Give the position of every leukocyte visible.
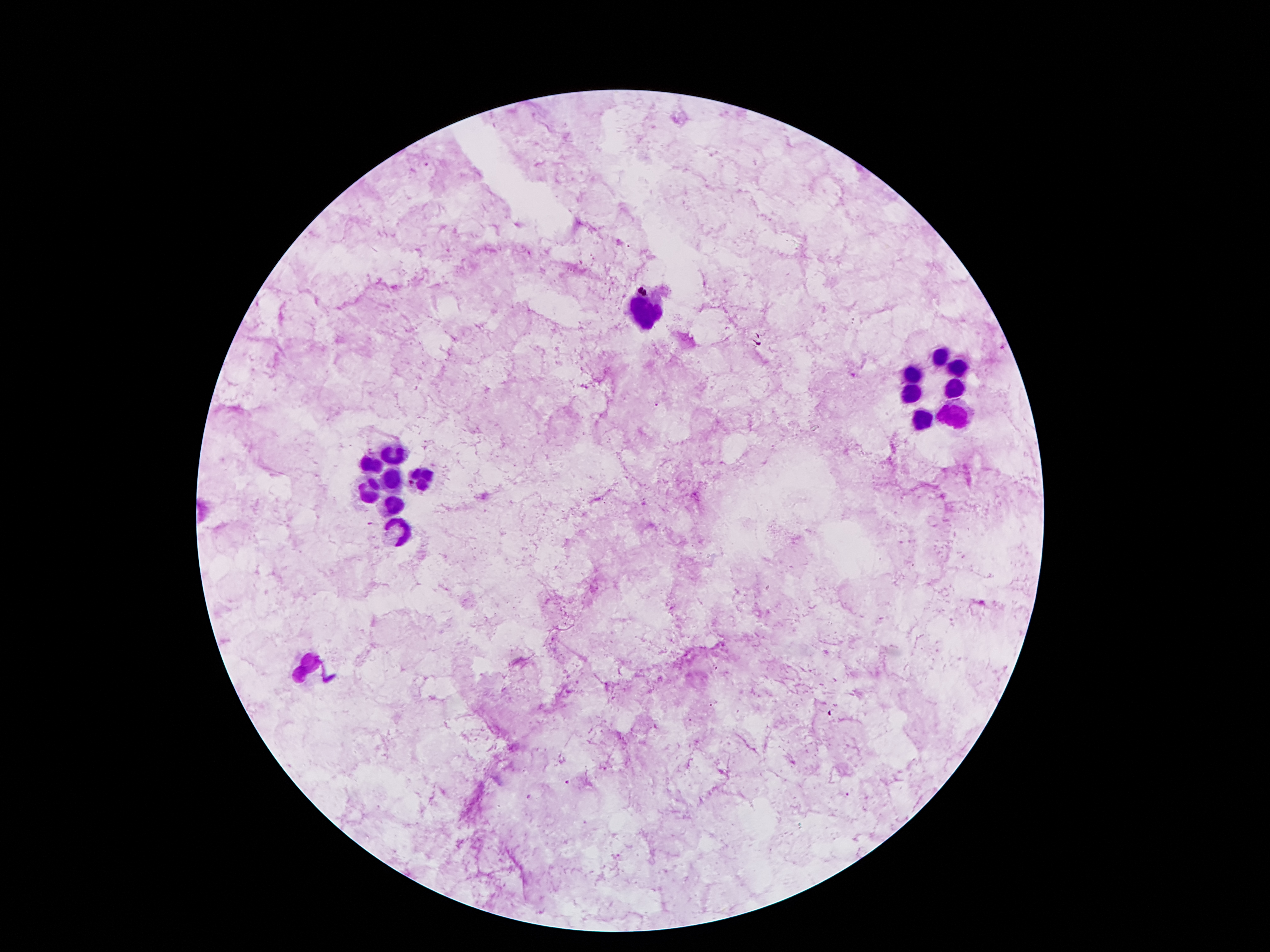

Approximate centers as (x, y) in pixels.
Leukocytes: (646, 312), (940, 356), (954, 370), (912, 373), (910, 391), (956, 391), (956, 410), (923, 417), (394, 457), (371, 461), (423, 478), (390, 480), (369, 492), (392, 505), (398, 530), (310, 666).

field_of_view: one from this slide
image_size: 1270×952 pixels
stain: Giemsa
capture: smartphone camera through the microscope eyepiece
malaria_parasite_locations: 'approximate centers as (x, y) in pixels: (428, 167), (1003, 347), (855, 374), (656, 403), (714, 668), (713, 703), (567, 783), (852, 792)'
patient_malaria_status: positive for Plasmodium falciparum
preparation: thick peripheral-blood smear
magnification: 100x